Assess this cell for malaria.
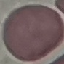
It is uninfected.

Summary:
  - Preparation: thin blood smear
  - Capture: smartphone through the microscope eyepiece
  - Image type: cell patch, automatically extracted from a larger field of view and resized to 64 × 64 pixels
  - Stain: Giemsa